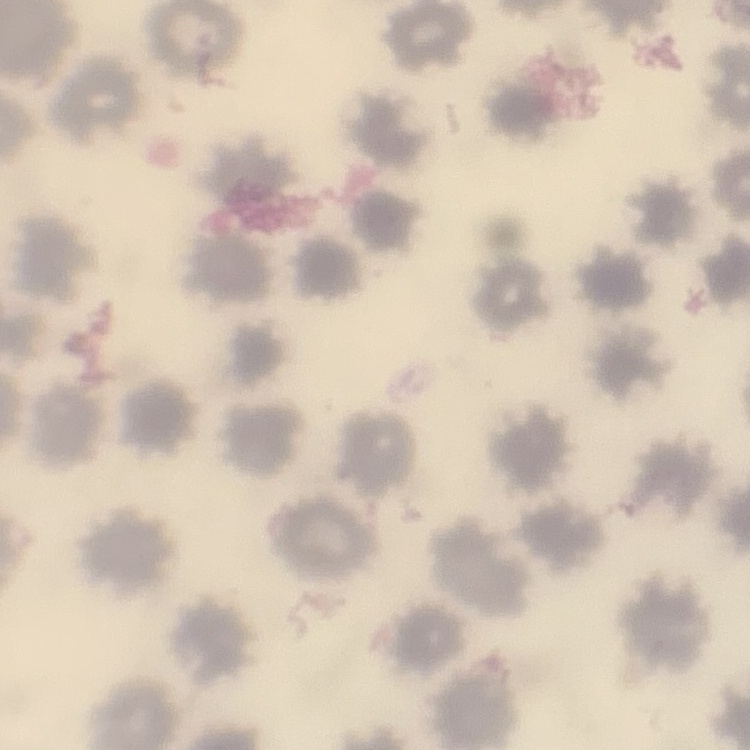

Summary:
  - Erythrocyte morphology: no rouleaux formation
  - Preparation: thin blood smear
  - Stain: Field's or Giemsa
  - Image type: square crop of a larger photomicrograph